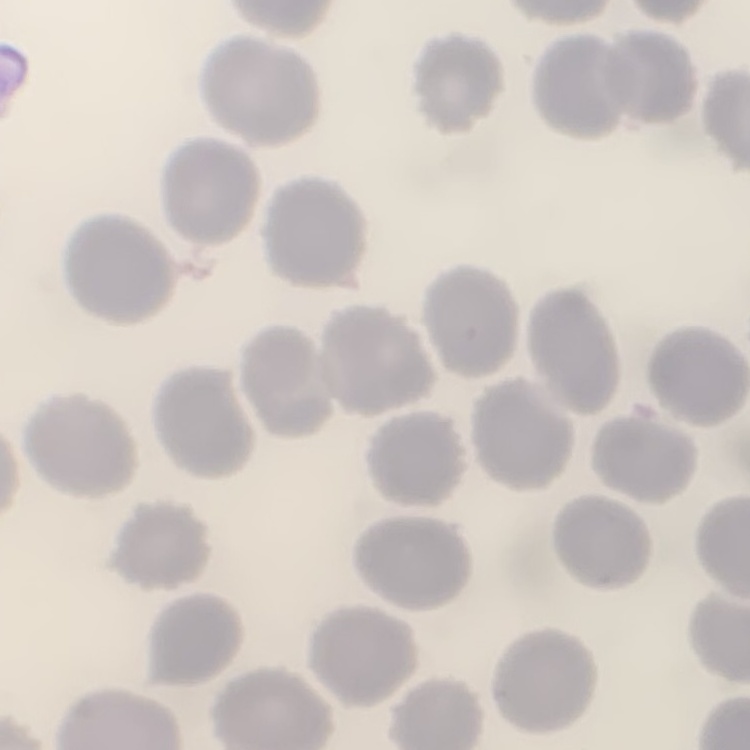
erythrocyte morphology = no rouleaux formation
stain = Field's or Giemsa
image type = one tile cut from a larger photomicrograph
preparation = thin blood film